Point out every malaria parasite and every leukocyte.
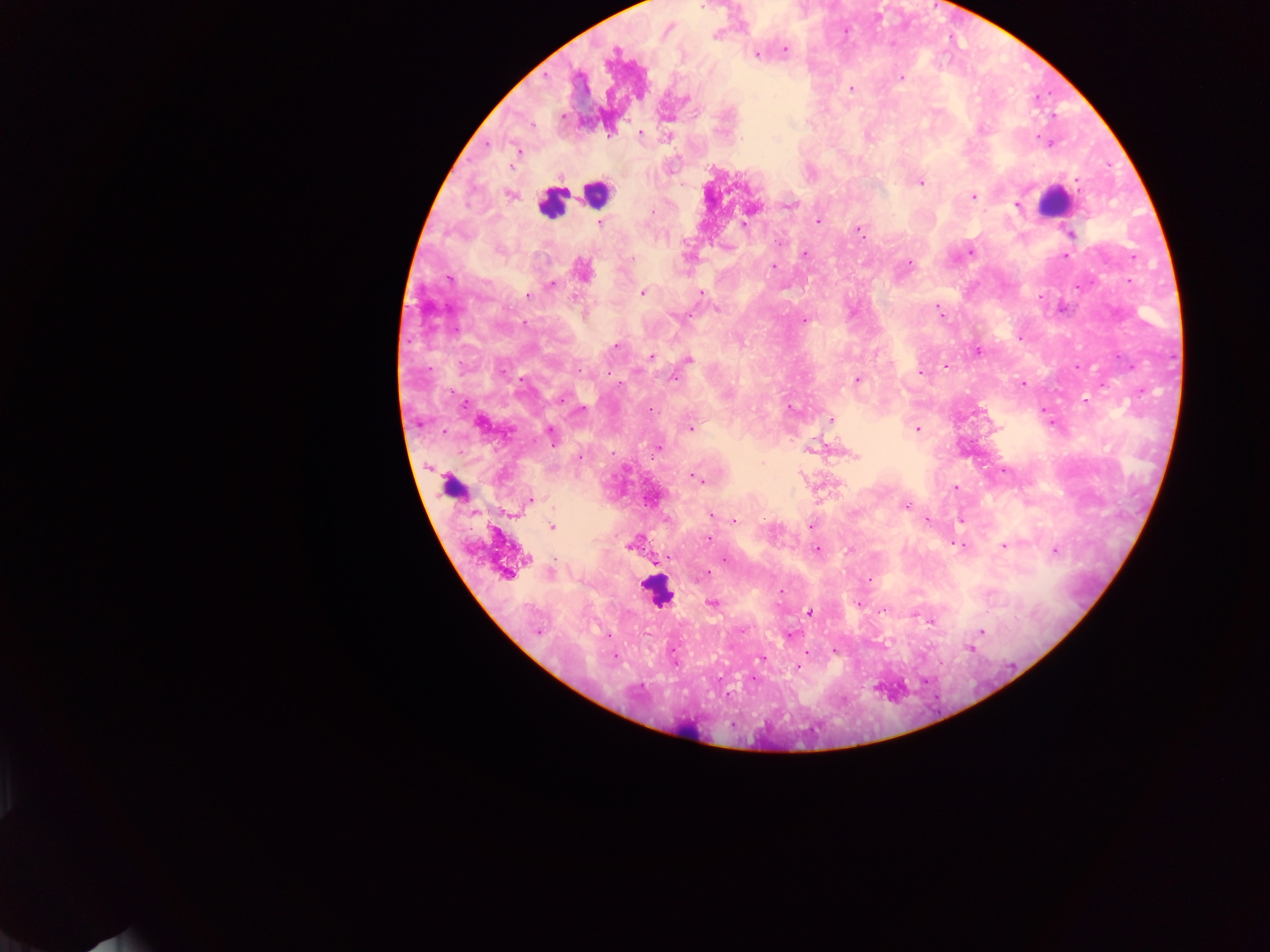

Approximate centers as (x, y) in pixels.
Malaria parasites: (703, 6), (716, 36), (785, 49), (756, 55), (612, 56), (901, 78), (850, 88), (610, 133), (640, 133), (518, 151), (921, 182), (1077, 182), (510, 195), (973, 197), (789, 205), (1016, 206), (652, 212), (818, 221), (600, 223), (743, 223), (859, 231), (1069, 234), (780, 242), (971, 253), (804, 254), (1067, 256), (632, 259), (909, 263), (774, 266), (582, 270), (448, 279), (552, 285), (641, 293), (701, 294), (528, 295), (717, 309), (938, 311), (804, 321), (1019, 337), (615, 347), (978, 351), (651, 356), (688, 358), (945, 366), (921, 373), (674, 379), (857, 380), (1022, 384), (1103, 385), (562, 398), (1086, 401), (790, 408), (580, 410), (650, 410), (830, 420), (479, 424), (691, 428), (917, 429), (551, 435), (657, 447), (811, 449), (854, 456), (579, 458), (698, 479), (956, 488), (531, 500), (906, 506), (711, 515), (927, 519), (735, 521), (812, 525), (552, 528), (709, 539), (958, 545), (629, 547), (1004, 547), (817, 549), (847, 550), (1054, 550), (526, 558), (725, 560), (660, 561), (551, 573), (506, 575), (704, 576), (870, 580), (712, 603), (858, 605), (884, 610), (810, 612), (930, 621), (538, 632), (981, 632), (608, 635), (790, 635), (969, 648), (834, 650), (614, 657), (760, 659), (676, 664), (797, 666).
Leukocytes: (596, 190), (1054, 202), (550, 203), (451, 487), (657, 591), (690, 728).

Summary:
  - Preparation: thick blood smear
  - Capture: mobile-phone photograph through a microscope
  - Field of view: single
  - Image size: 1270×952 pixels
  - Country: Ghana